Point out each leukocyte.
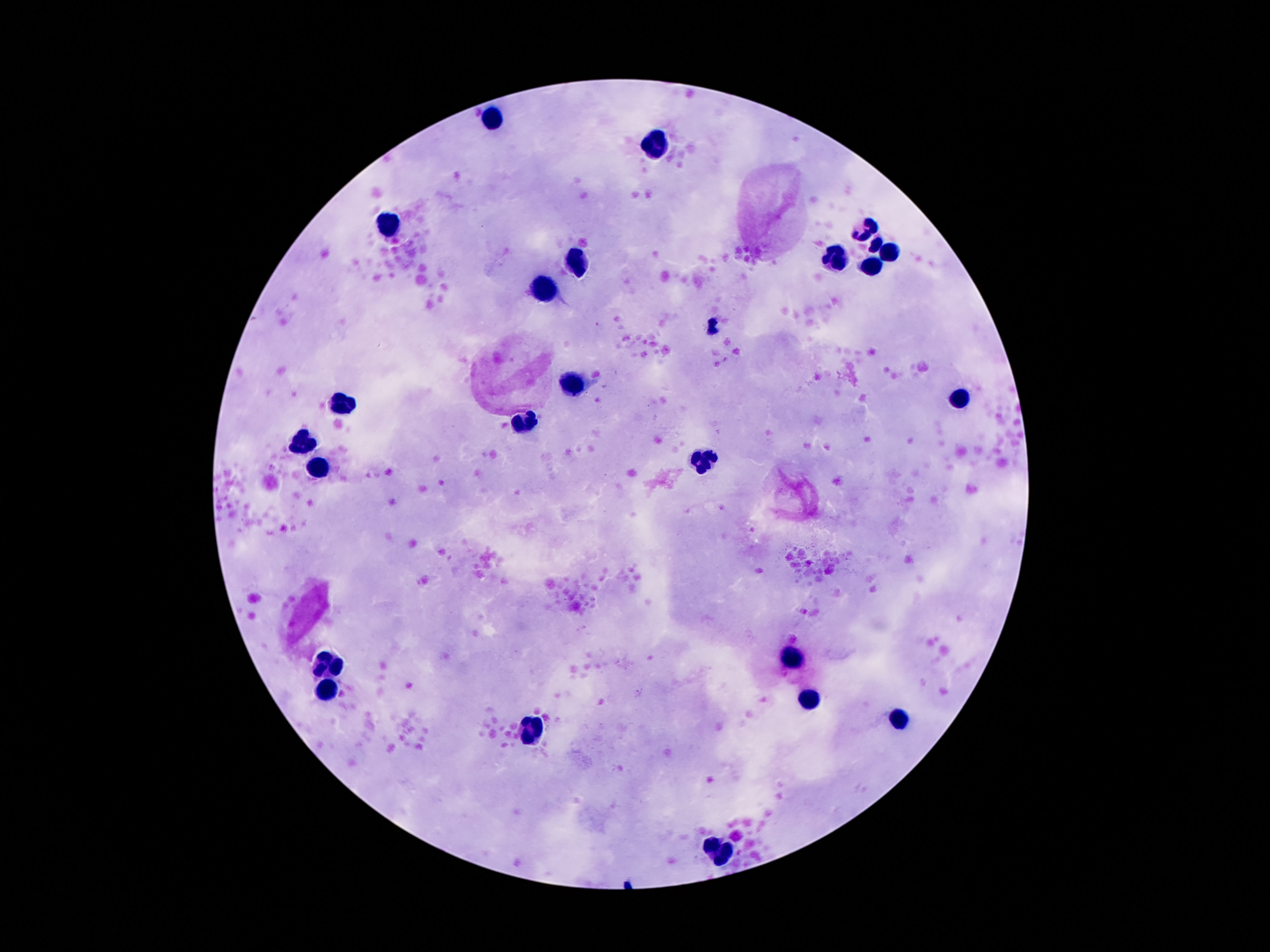
Approximate centers as {x, y} in pixels.
Leukocytes: {493, 115}, {656, 148}, {865, 225}, {391, 229}, {876, 246}, {891, 252}, {835, 257}, {576, 262}, {871, 267}, {542, 285}, {713, 324}, {576, 383}, {955, 397}, {340, 404}, {525, 427}, {305, 442}, {704, 464}, {320, 466}, {326, 661}, {790, 662}, {324, 686}, {807, 701}, {899, 715}, {534, 730}, {720, 850}.

Summary:
  - Patient malaria status: negative
  - Magnification: 100x
  - Stain: Giemsa
  - Image size: 1270×952 pixels
  - Field of view: one from this slide
  - Preparation: thick blood film
  - Capture: smartphone camera through the microscope eyepiece